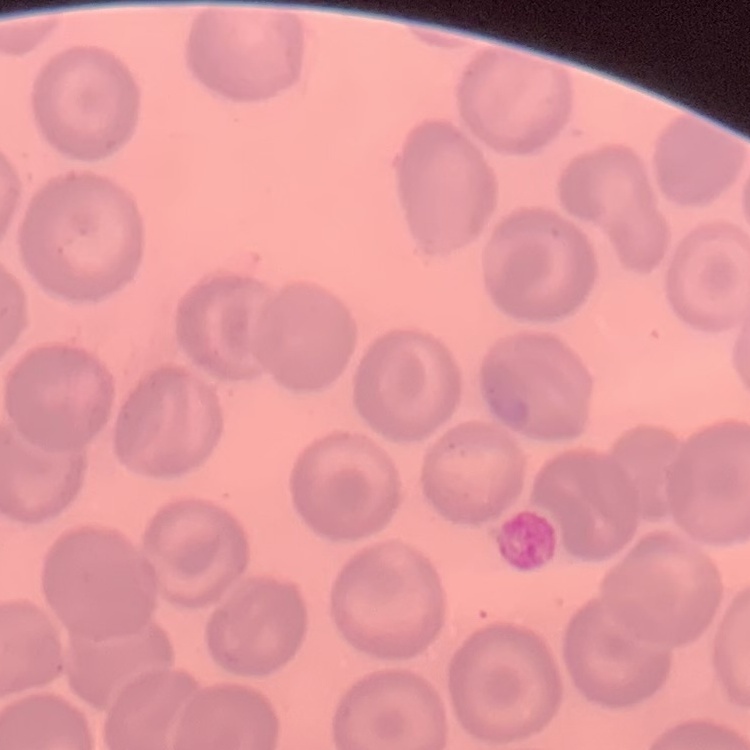

Summary:
  - Red blood cell morphology: no rouleaux formation
  - Preparation: thin blood smear
  - Image type: square crop of a larger photomicrograph
  - Stain: Field's or Giemsa